Locate malaria parasites and leukocytes.
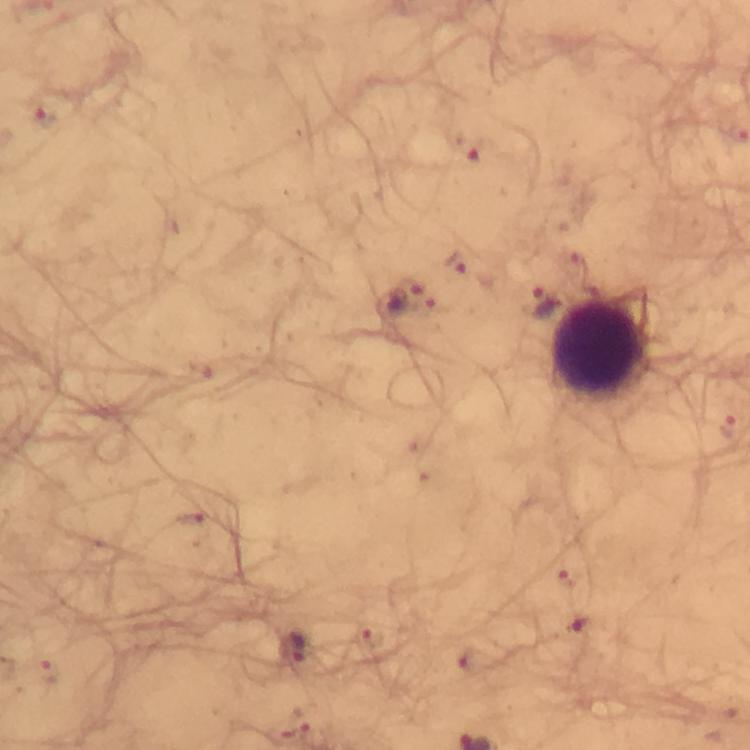

Approximate centers as [x, y] in pixels.
Malaria parasites: [470, 146], [456, 260], [410, 296], [544, 302], [728, 428], [291, 647].
Leukocytes: [602, 349].

Summary:
  - Stain: Giemsa
  - Image size: 750×750 pixels
  - Magnification: 100x
  - Cropped from: one field of view
  - Immersion oil: used
  - Capture: smartphone mounted on the microscope
  - Preparation: thick blood film
  - Context: from a malaria diagnostic workup